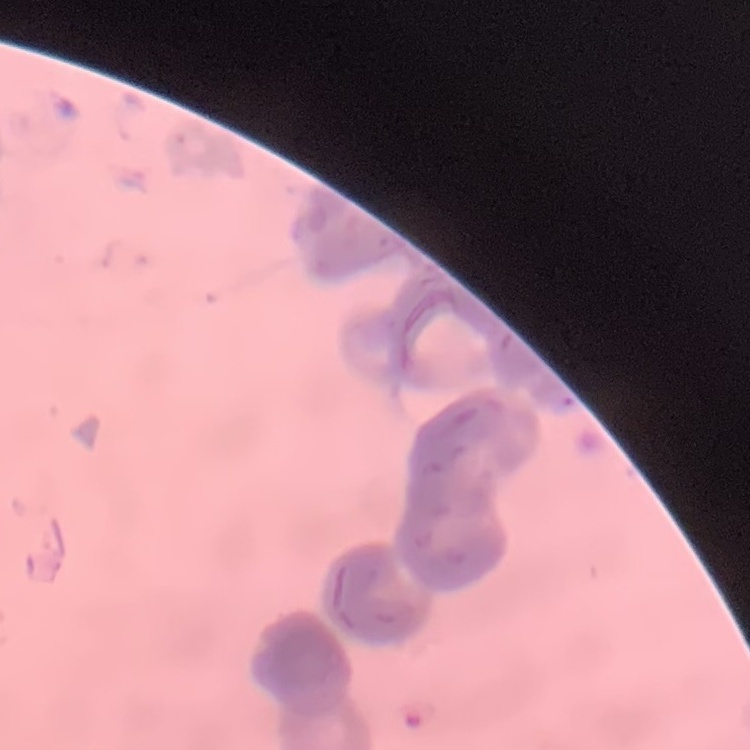
The erythrocytes exhibit rouleaux formation. Stained with either Field's or Giemsa. One tile cut from a larger photomicrograph. Thin blood film.